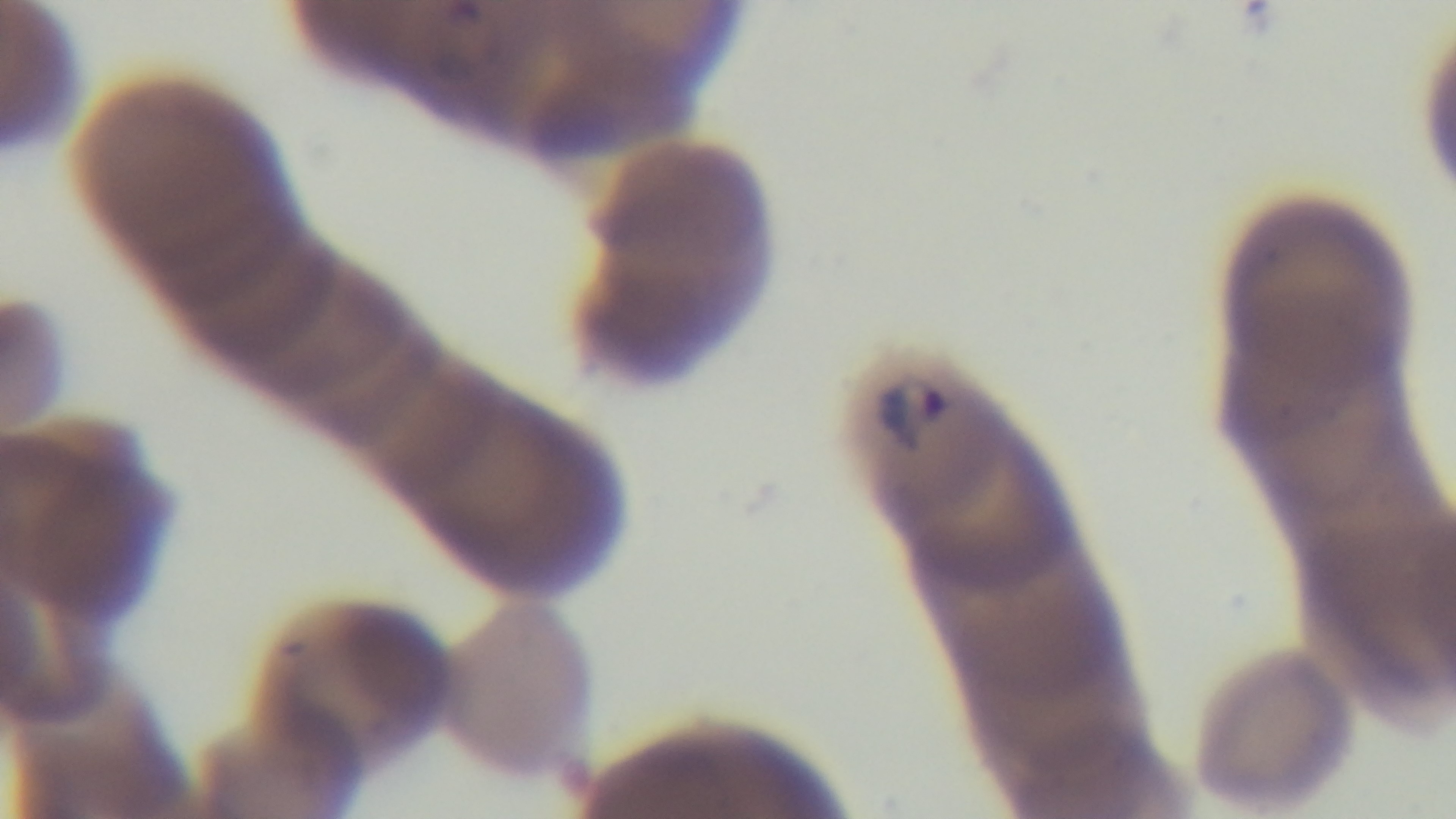
Malaria status: positive. Oil-immersion objective, 100x. Giemsa stain. Preparation: thin. Captured with a mounted 4K digital camera. Photomicrograph. Single field of view.